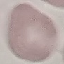
malaria status = uninfected
capture = smartphone through the microscope eyepiece
stain = Giemsa
image type = cell patch, automatically extracted from a larger field of view and resized to 64 × 64 pixels
preparation = thin blood smear